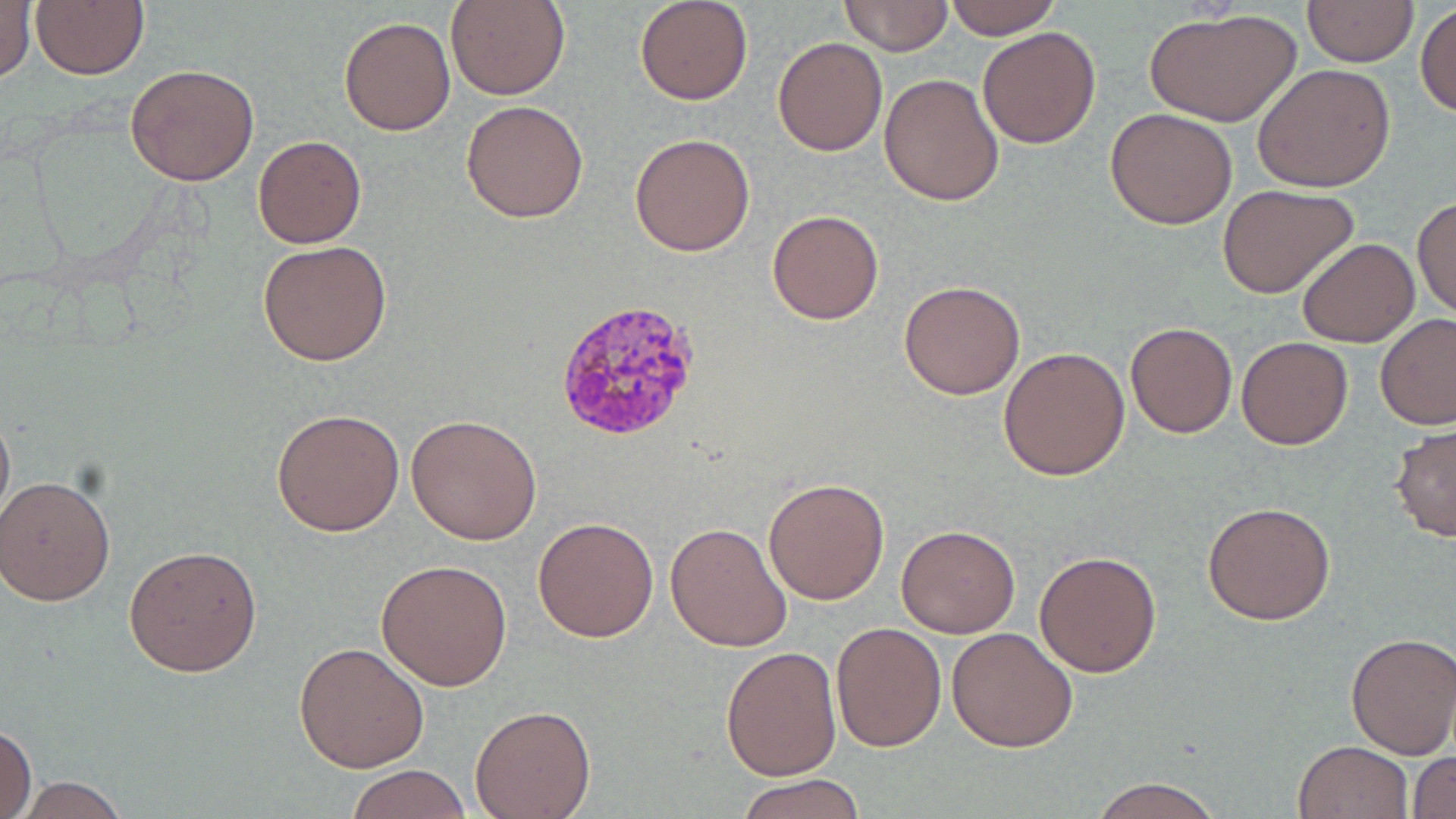
Summary:
  - Coordinate format: approximate bounding boxes as named x1/y1/x2/y2 corners in pixels
  - Uninfected red blood cell locations: (x1=446, y1=0, x2=569, y2=101), (x1=636, y1=0, x2=752, y2=104), (x1=838, y1=0, x2=953, y2=54), (x1=945, y1=0, x2=1061, y2=40), (x1=0, y1=1, x2=35, y2=85), (x1=1302, y1=1, x2=1419, y2=67), (x1=29, y1=2, x2=149, y2=79), (x1=1415, y1=3, x2=1456, y2=117), (x1=1146, y1=8, x2=1300, y2=130), (x1=338, y1=16, x2=455, y2=136), (x1=977, y1=26, x2=1103, y2=148), (x1=773, y1=36, x2=887, y2=156), (x1=1252, y1=63, x2=1396, y2=193), (x1=126, y1=64, x2=259, y2=186), (x1=879, y1=72, x2=1005, y2=207), (x1=461, y1=99, x2=589, y2=222), (x1=1105, y1=108, x2=1237, y2=229), (x1=629, y1=133, x2=758, y2=256), (x1=253, y1=135, x2=366, y2=247), (x1=1218, y1=184, x2=1357, y2=298), (x1=1412, y1=194, x2=1456, y2=320), (x1=768, y1=209, x2=883, y2=326), (x1=1297, y1=238, x2=1417, y2=348), (x1=257, y1=240, x2=394, y2=367), (x1=899, y1=278, x2=1027, y2=401), (x1=1376, y1=315, x2=1456, y2=431), (x1=1124, y1=320, x2=1239, y2=438), (x1=1236, y1=336, x2=1352, y2=450), (x1=999, y1=347, x2=1130, y2=482), (x1=0, y1=402, x2=14, y2=531), (x1=271, y1=407, x2=404, y2=538), (x1=405, y1=413, x2=542, y2=545), (x1=1391, y1=423, x2=1455, y2=543), (x1=0, y1=474, x2=116, y2=605), (x1=763, y1=478, x2=891, y2=604), (x1=1202, y1=500, x2=1337, y2=625), (x1=532, y1=516, x2=658, y2=643), (x1=666, y1=521, x2=791, y2=653), (x1=896, y1=525, x2=1019, y2=638), (x1=123, y1=544, x2=262, y2=677), (x1=1034, y1=550, x2=1162, y2=678), (x1=377, y1=558, x2=512, y2=689), (x1=830, y1=622, x2=945, y2=753), (x1=946, y1=627, x2=1078, y2=751), (x1=1345, y1=632, x2=1456, y2=758), (x1=293, y1=641, x2=429, y2=774), (x1=720, y1=645, x2=841, y2=780), (x1=469, y1=705, x2=595, y2=819), (x1=0, y1=723, x2=37, y2=819), (x1=1292, y1=739, x2=1414, y2=819), (x1=1409, y1=751, x2=1456, y2=819), (x1=345, y1=764, x2=472, y2=819), (x1=739, y1=772, x2=865, y2=819), (x1=1086, y1=775, x2=1225, y2=818), (x1=10, y1=776, x2=132, y2=818)
  - Plasmodium vivax-infected red blood cell locations: (x1=553, y1=296, x2=705, y2=442)
  - Slide-level diagnosis: Plasmodium vivax
  - Field of view: one of a larger specimen
  - Magnification: 1000x
  - Image size: 1456×819 pixels
  - Modality: light microscopy
  - Preparation: thin blood smear
  - Stain: May-Grünwald-Giemsa